Give the position of every Plasmodium parasite visible.
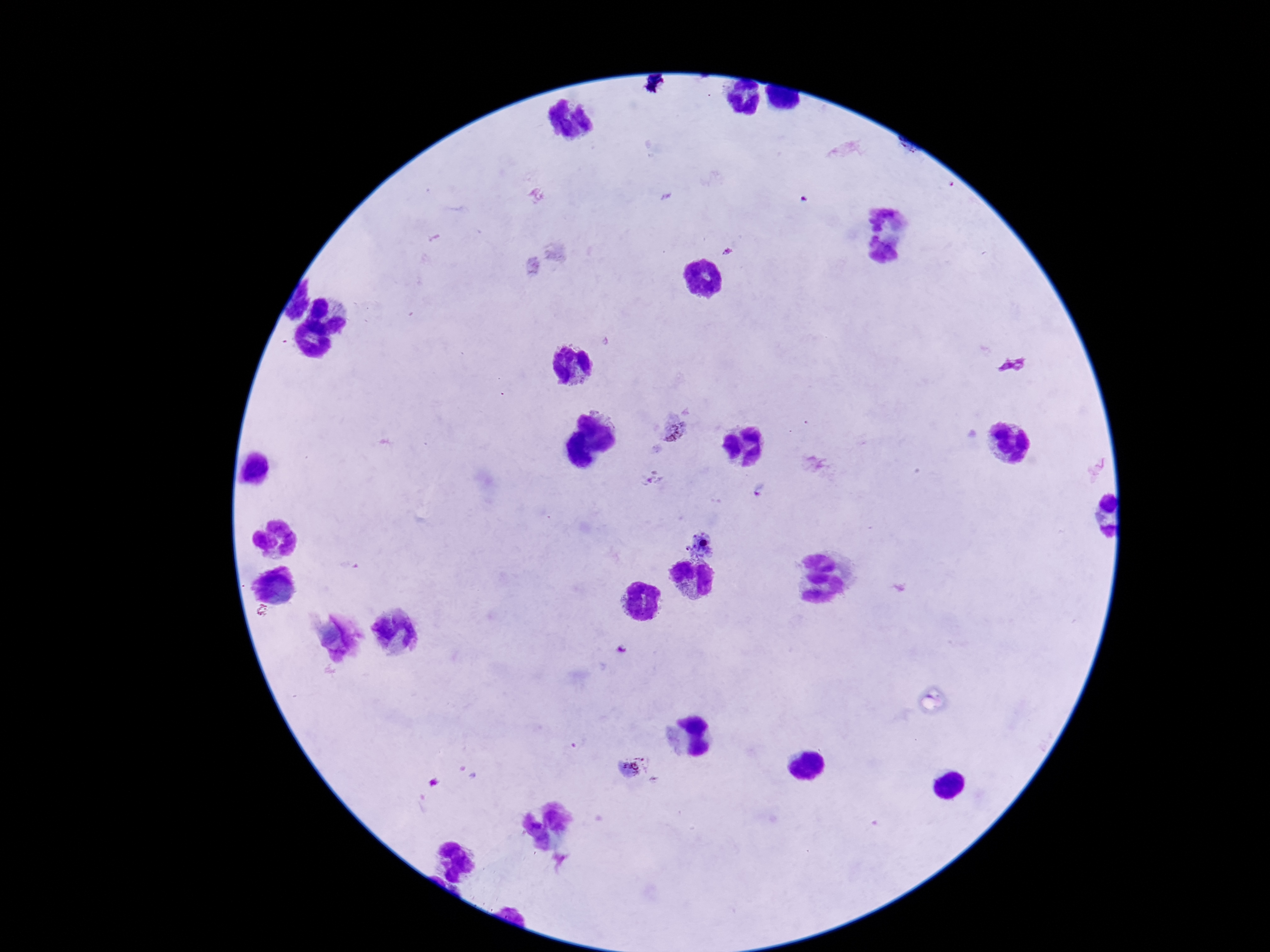
Approximate centers as [x, y] in pixels.
Plasmodium parasites: [675, 426], [653, 479], [761, 489], [703, 545], [631, 766].

Summary:
  - Field of view: single
  - Preparation: thick blood smear
  - Image size: 1270×952 pixels
  - Magnification: 100x
  - Stain: Giemsa
  - Patient malaria status: positive
  - Capture: smartphone camera through the microscope eyepiece